Report the malaria status of this cell.
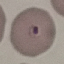
It is parasitized.

Thin blood film. Giemsa-stained preparation. Acquired by smartphone through the microscope eyepiece. Cell patch, automatically extracted from a larger field of view and resized to 64 × 64 pixels.